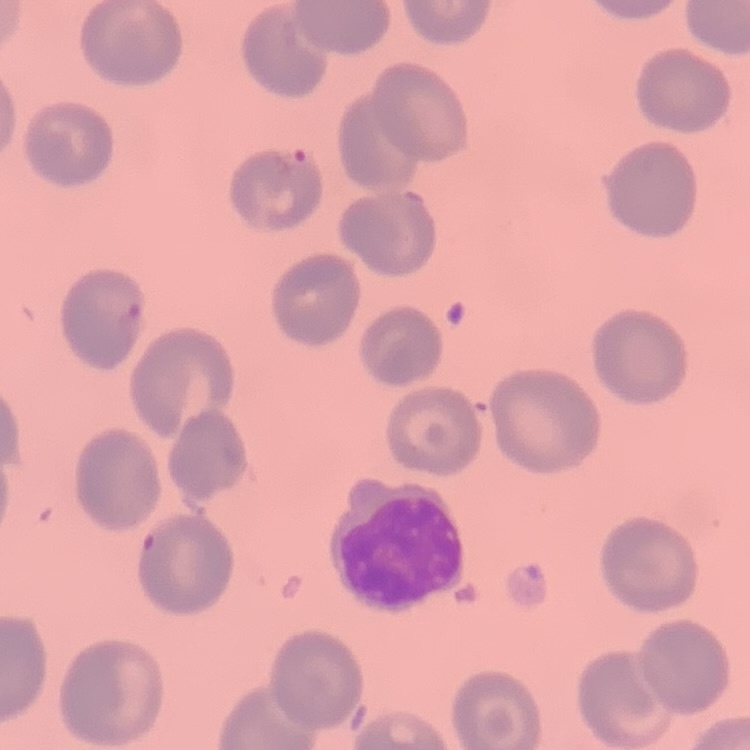
Summary:
  - Erythrocyte morphology: no rouleaux formation
  - Preparation: thin blood film
  - Stain: Field's or Giemsa
  - Image type: square crop of a larger photomicrograph